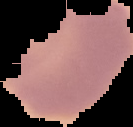
image size = 133×127 pixels
preparation = thin blood film
result = negative for Plasmodium parasites
image type = segmented cell region with the area outside set to black